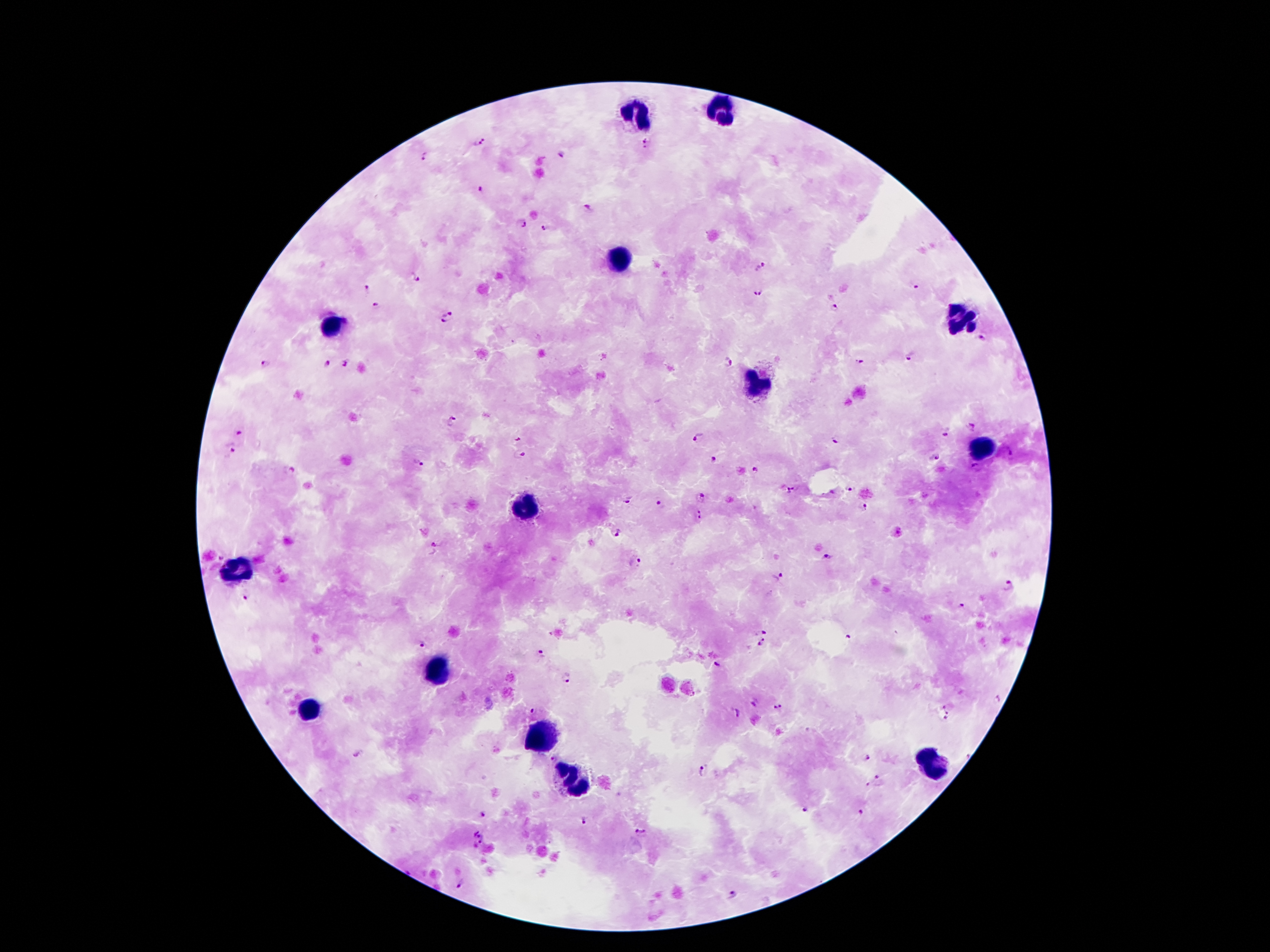 Approximate centers as {x, y} in pixels. Malaria parasite locations: {480, 141}, {645, 144}, {561, 154}, {424, 156}, {480, 189}, {585, 208}, {522, 224}, {543, 229}, {762, 266}, {416, 277}, {916, 287}, {368, 288}, {758, 292}, {377, 306}, {834, 309}, {446, 312}, {444, 322}, {983, 337}, {909, 359}, {727, 362}, {859, 362}, {346, 363}, {265, 364}, {328, 364}, {452, 419}, {970, 425}, {945, 430}, {238, 433}, {696, 436}, {835, 439}, {520, 440}, {234, 450}, {1009, 453}, {518, 456}, {934, 457}, {713, 460}, {417, 463}, {292, 469}, {976, 469}, {755, 470}, {790, 488}, {847, 488}, {701, 495}, {627, 500}, {659, 505}, {863, 509}, {701, 515}, {615, 532}, {437, 545}, {827, 557}, {222, 558}, {636, 563}, {778, 577}, {1008, 584}, {246, 597}, {962, 607}, {759, 630}, {846, 636}, {762, 643}, {422, 644}, {540, 653}, {716, 664}, {567, 678}, {999, 698}, {754, 704}, {777, 707}, {944, 707}, {537, 710}, {739, 713}, {948, 713}, {945, 718}, {360, 753}, {867, 757}, {554, 759}, {704, 769}, {878, 778}, {868, 786}, {805, 807}, {860, 813}, {484, 816}, {584, 821}, {478, 833}, {642, 834}, {479, 846}, {462, 886}, {733, 896}. Leukocyte locations: {724, 109}, {635, 114}, {623, 261}, {961, 320}, {331, 327}, {756, 386}, {984, 446}, {524, 506}, {240, 571}, {435, 673}, {309, 706}, {541, 734}, {934, 765}, {573, 782}. Thick blood film. 100x magnification. Patient malaria status: positive for Plasmodium falciparum. Giemsa-stained preparation. Single field of view. Smartphone photograph taken through the microscope eyepiece. Image is 1270×952 pixels.